Outline each blood parasite and name the species.
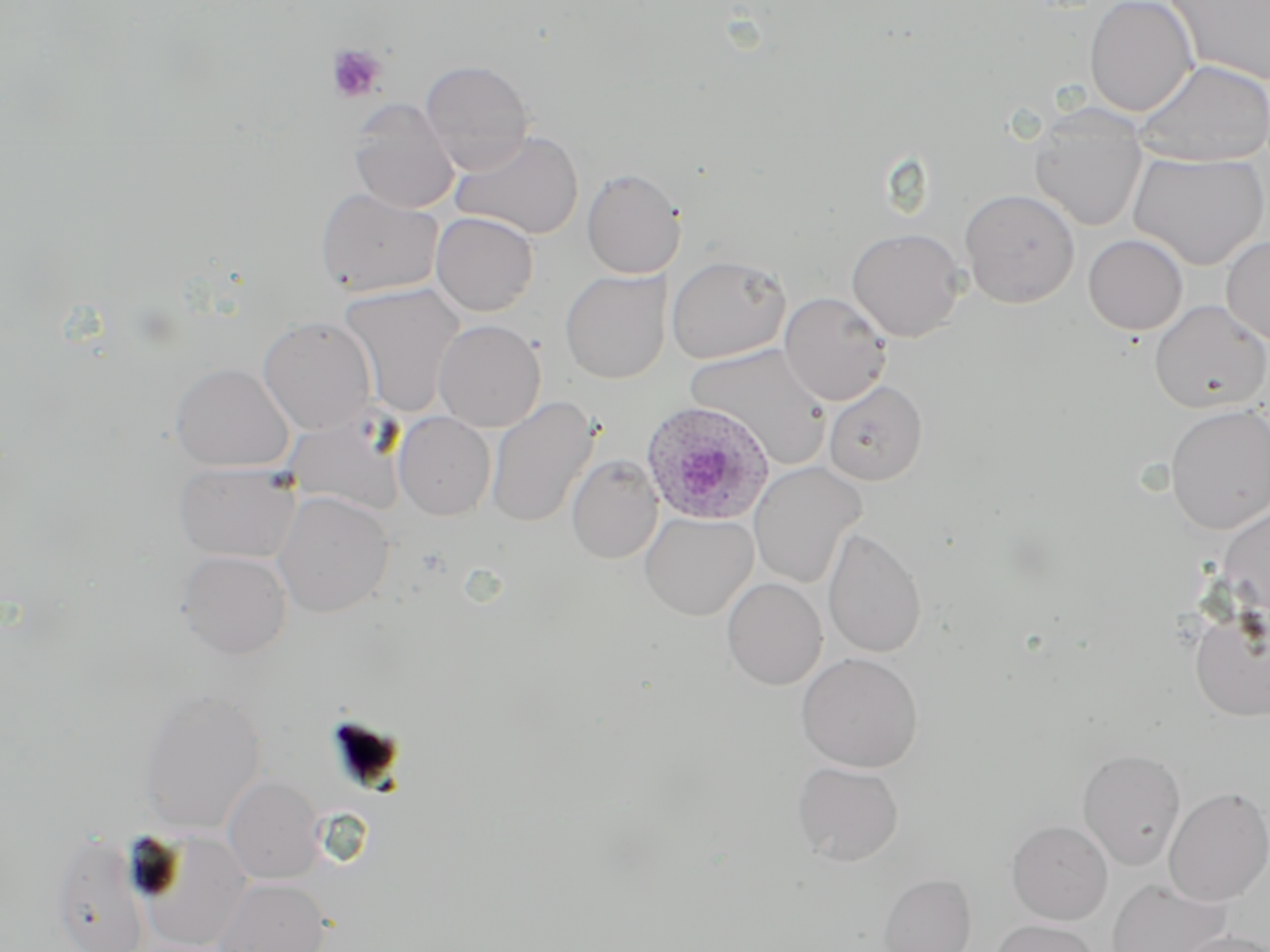

Approximate bounding boxes as [x1, y1, x2, y2] in pixels.
Plasmodium ovale-infected red blood cells: [641, 401, 773, 526].
No Plasmodium falciparum, Plasmodium malariae, Plasmodium vivax, Babesia divergens, or Trypanosoma brucei observed.

Platelet locations: [325, 43, 387, 103]. Uninfected red blood cell locations: [1084, 0, 1199, 117], [1166, 0, 1270, 86], [418, 59, 536, 171], [1134, 59, 1270, 167], [349, 100, 459, 214], [1029, 107, 1148, 232], [450, 129, 585, 240], [1127, 151, 1269, 270], [581, 168, 685, 279], [316, 188, 443, 298], [958, 188, 1080, 308], [431, 212, 539, 316], [846, 228, 966, 342], [1083, 234, 1188, 336], [1221, 236, 1270, 346], [666, 254, 790, 363], [560, 269, 671, 384], [339, 283, 465, 417], [779, 291, 893, 406], [1149, 300, 1269, 413], [258, 315, 378, 435], [433, 319, 546, 432], [685, 343, 831, 468], [170, 362, 294, 472], [823, 380, 927, 485], [485, 396, 599, 529], [1164, 404, 1270, 534], [394, 412, 496, 520], [284, 413, 407, 516], [566, 455, 663, 564], [174, 461, 301, 562], [749, 462, 866, 589], [272, 491, 395, 618], [1217, 503, 1270, 622], [639, 511, 758, 620], [823, 526, 927, 659], [177, 549, 293, 659], [722, 577, 827, 690], [1189, 603, 1269, 723], [796, 651, 923, 772], [137, 685, 267, 834], [1076, 747, 1186, 870], [791, 760, 904, 866], [224, 774, 324, 884], [1162, 786, 1270, 906], [1006, 820, 1113, 924], [50, 831, 149, 952], [139, 832, 253, 951], [879, 873, 977, 952], [1106, 877, 1232, 952], [214, 878, 332, 952], [988, 918, 1102, 952], [1171, 929, 1270, 952]. Slide-level diagnosis: Plasmodium ovale. Optical microscopy. Image is 1270×952 pixels. Thin blood smear. Captured at 1000x magnification. May-Grünwald-Giemsa stain. One field of a larger specimen.